Give the extent of all Plasmodium ovale-infected red blood cells.
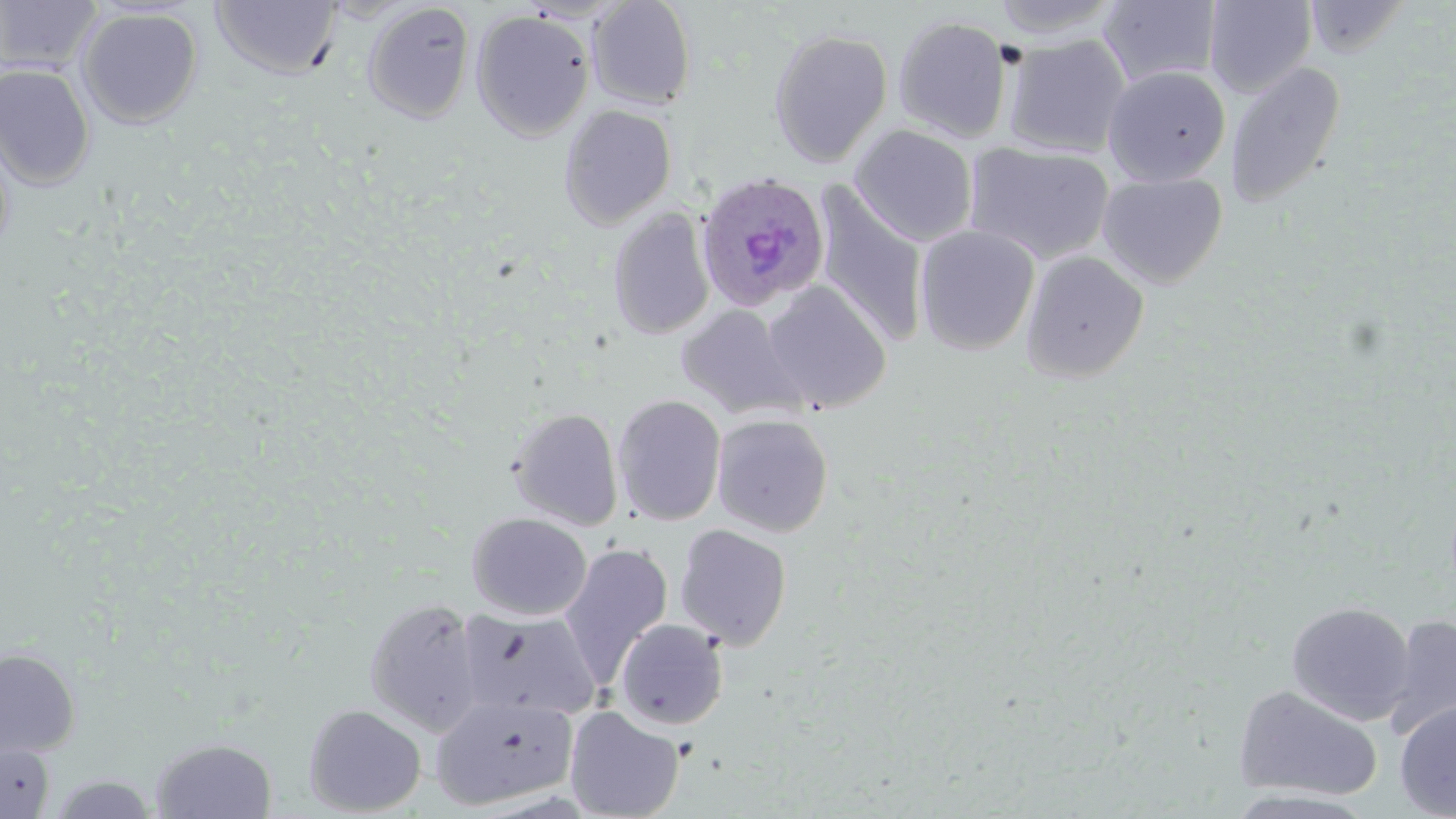

Approximate bounding boxes as (x1, y1, x2, y2) in pixels.
Plasmodium ovale-infected red blood cells: (695, 171, 831, 313).

Uninfected red blood cell locations: (0, 0, 102, 74), (587, 0, 697, 110), (989, 0, 1123, 39), (1203, 0, 1317, 97), (210, 1, 343, 80), (1098, 1, 1222, 89), (1305, 1, 1411, 57), (363, 2, 475, 124), (76, 7, 203, 128), (471, 9, 595, 141), (893, 15, 1013, 142), (768, 27, 893, 167), (1003, 34, 1131, 158), (1224, 61, 1346, 208), (0, 63, 96, 189), (1102, 65, 1231, 186), (558, 104, 677, 229), (849, 124, 979, 247), (0, 130, 15, 259), (965, 142, 1115, 266), (1097, 171, 1228, 288), (813, 185, 930, 350), (608, 208, 715, 341), (915, 225, 1040, 355), (1020, 250, 1150, 383), (761, 281, 892, 413), (676, 303, 807, 421), (613, 394, 726, 526), (508, 407, 624, 531), (712, 413, 834, 538), (467, 512, 592, 621), (674, 524, 792, 652), (558, 542, 674, 686), (364, 598, 484, 736), (1286, 601, 1415, 726), (458, 608, 600, 720), (1383, 614, 1456, 742), (614, 618, 729, 730), (0, 648, 81, 758), (1233, 683, 1383, 801), (431, 693, 578, 810), (1394, 699, 1456, 818), (304, 704, 427, 816), (564, 705, 685, 819), (150, 737, 278, 818), (0, 742, 56, 817), (47, 773, 160, 818). Slide-level diagnosis: Plasmodium ovale. Thin blood film. May-Grünwald-Giemsa stain. Light microscopy. Captured at 1000x magnification. Image is 1456×819 pixels. Single field of view.